Locate and identify every blood parasite.
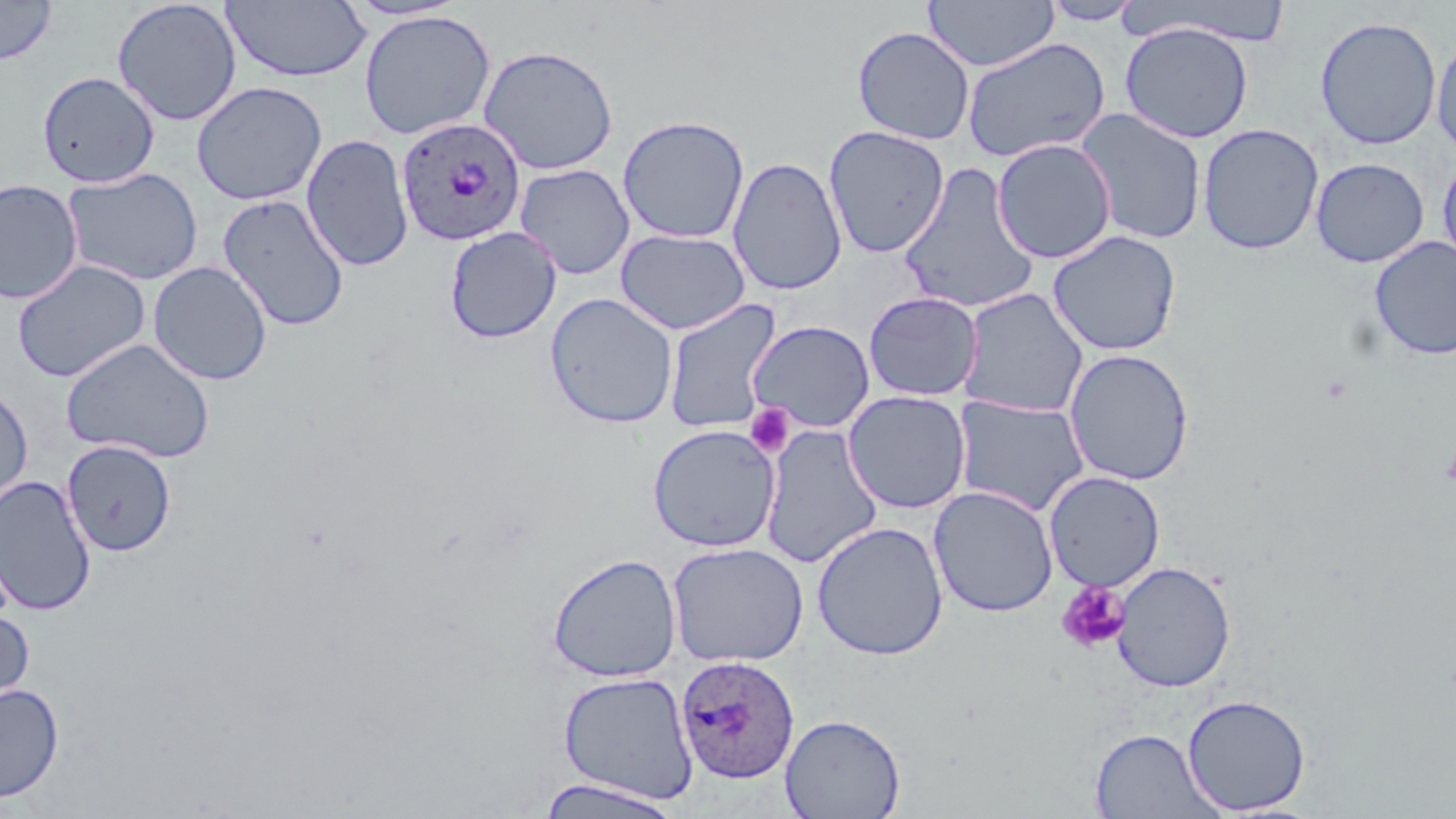

Approximate bounding boxes as (x1, y1, x2, y2) in pixels.
Plasmodium ovale-infected red blood cells: (396, 117, 526, 248), (676, 654, 800, 783).
No Plasmodium falciparum, Plasmodium malariae, Plasmodium vivax, Babesia divergens, or Trypanosoma brucei observed.

Platelet locations: (745, 403, 793, 457), (1441, 439, 1456, 492), (1055, 581, 1130, 653). Uninfected red blood cell locations: (924, 0, 1059, 72), (1041, 0, 1145, 26), (0, 1, 57, 64), (112, 1, 242, 127), (221, 1, 371, 83), (1122, 2, 1293, 45), (359, 10, 495, 140), (1314, 15, 1442, 151), (1119, 22, 1254, 143), (852, 26, 975, 145), (1431, 34, 1456, 160), (962, 37, 1111, 163), (478, 45, 619, 175), (37, 71, 159, 188), (191, 81, 327, 206), (1074, 107, 1207, 245), (617, 115, 750, 244), (1198, 123, 1324, 255), (823, 126, 950, 258), (301, 134, 415, 272), (991, 138, 1117, 264), (1437, 154, 1456, 273), (727, 156, 848, 296), (1311, 157, 1429, 268), (898, 162, 1039, 314), (515, 163, 635, 280), (62, 167, 203, 286), (0, 178, 83, 304), (218, 193, 350, 332), (445, 226, 561, 343), (616, 229, 750, 335), (1047, 230, 1182, 356), (1370, 235, 1456, 360), (11, 260, 151, 382), (148, 261, 272, 386), (958, 288, 1088, 418), (863, 291, 983, 401), (545, 292, 678, 428), (663, 298, 781, 433), (748, 320, 876, 433), (60, 337, 216, 463), (1063, 348, 1195, 486), (0, 384, 34, 510), (843, 390, 971, 514), (952, 395, 1091, 517), (647, 424, 780, 552), (761, 425, 884, 568), (62, 440, 177, 557), (1044, 471, 1165, 592), (0, 475, 97, 616), (929, 486, 1059, 618), (812, 521, 949, 659), (667, 541, 808, 668), (547, 552, 681, 682), (1112, 560, 1236, 693), (0, 605, 35, 712), (558, 671, 698, 804), (0, 682, 64, 804), (1182, 694, 1311, 815), (781, 713, 906, 818), (1090, 728, 1222, 818), (534, 777, 683, 818). Slide-level diagnosis: Plasmodium ovale. Light microscopy. Captured at 1000x magnification. May-Grünwald-Giemsa-stained preparation. Thin blood smear. Single field of view. Image is 1456×819 pixels.